Name the blood parasite species.
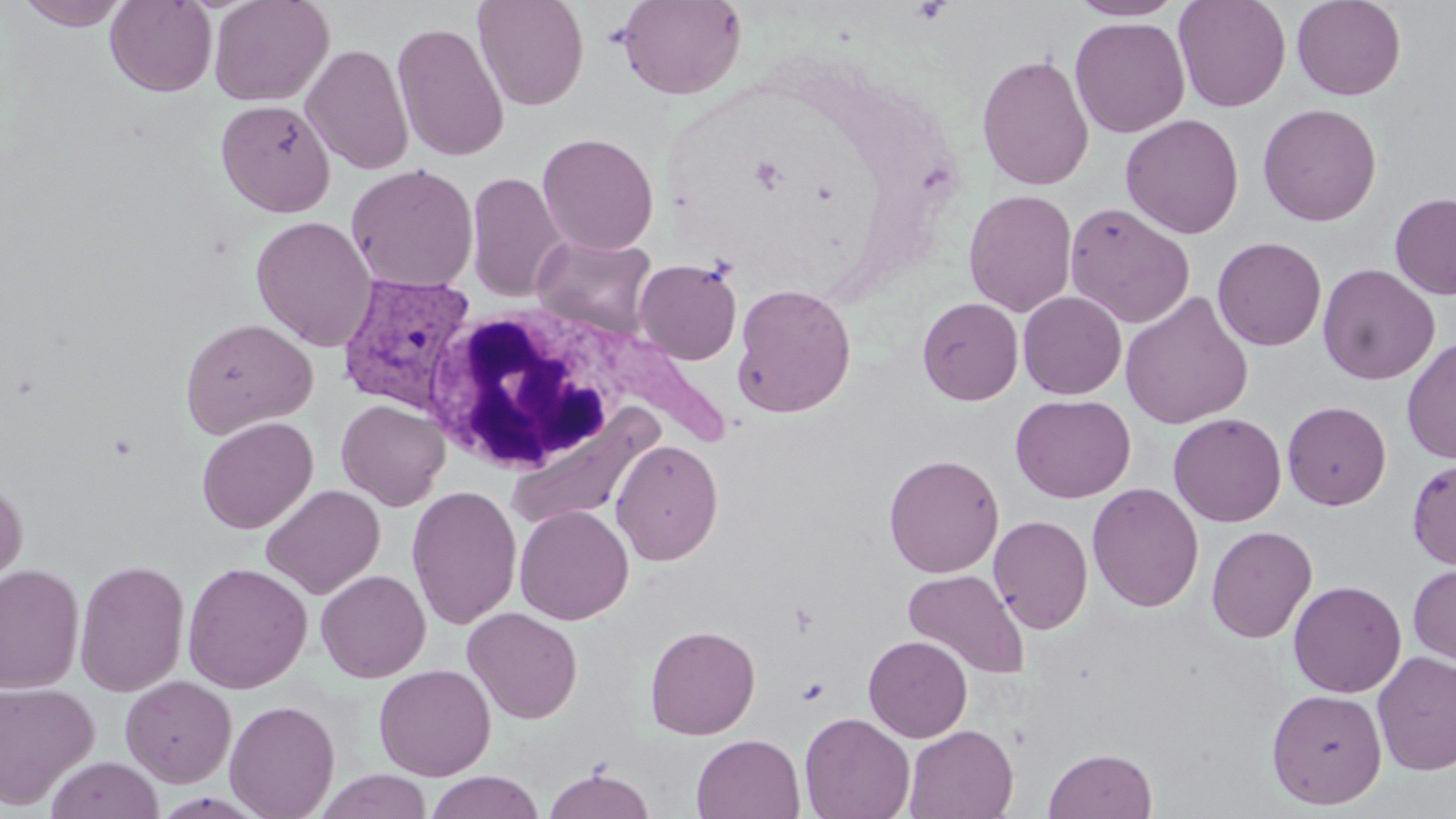

Plasmodium vivax.

Summary:
  - Coordinate format: approximate bounding boxes as (x1, y1, x2, y2) in pixels
  - White blood cell locations: (422, 304, 639, 478)
  - Uninfected red blood cell locations: (14, 0, 132, 29), (105, 0, 217, 97), (209, 0, 334, 107), (473, 0, 589, 111), (617, 0, 746, 100), (1068, 0, 1186, 21), (1173, 0, 1291, 112), (1291, 0, 1406, 100), (1070, 16, 1190, 138), (391, 21, 509, 162), (301, 42, 414, 176), (976, 52, 1094, 191), (216, 99, 336, 217), (1257, 103, 1382, 226), (1120, 113, 1244, 239), (536, 132, 659, 255), (345, 163, 479, 292), (466, 171, 570, 303), (963, 189, 1078, 317), (1390, 192, 1456, 300), (1063, 202, 1195, 327), (250, 215, 377, 352), (531, 234, 659, 339), (1212, 236, 1327, 351), (634, 258, 742, 365), (1318, 263, 1440, 385), (732, 283, 856, 418), (1018, 291, 1126, 399), (1119, 291, 1254, 429), (917, 297, 1023, 405), (180, 317, 318, 439), (1401, 336, 1456, 465), (1010, 394, 1135, 503), (336, 399, 451, 511), (1282, 401, 1392, 510), (505, 405, 664, 535), (1168, 412, 1287, 527), (196, 416, 318, 534), (610, 439, 724, 566), (883, 453, 1004, 578), (1407, 457, 1456, 570), (0, 475, 29, 603), (1087, 482, 1204, 612), (260, 483, 386, 599), (406, 485, 522, 630), (514, 505, 633, 625), (989, 515, 1093, 635), (1206, 525, 1317, 644), (74, 558, 191, 697), (1408, 560, 1456, 666), (0, 562, 84, 694), (182, 562, 312, 694), (902, 568, 1030, 680), (316, 569, 431, 683), (1288, 580, 1406, 698), (462, 607, 583, 724), (645, 624, 761, 739), (863, 635, 973, 742), (1372, 651, 1456, 776), (373, 664, 496, 780), (121, 675, 237, 787), (0, 680, 100, 809), (1266, 688, 1388, 809), (224, 699, 340, 819), (799, 711, 916, 819), (903, 724, 1018, 818), (691, 733, 806, 819), (1043, 747, 1158, 818), (44, 756, 163, 819), (543, 766, 656, 819), (314, 770, 434, 819), (424, 770, 545, 819)
  - Platelet locations: (797, 677, 829, 705)
  - Plasmodium vivax-infected red blood cell locations: (335, 272, 479, 417)
  - Magnification: 1000x
  - Image size: 1456×819 pixels
  - Field of view: one of a larger specimen
  - Stain: May-Grünwald-Giemsa
  - Modality: optical microscopy
  - Preparation: thin blood smear